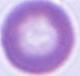

identification: erythrocyte
modality: photomicrograph
magnification: 1000x